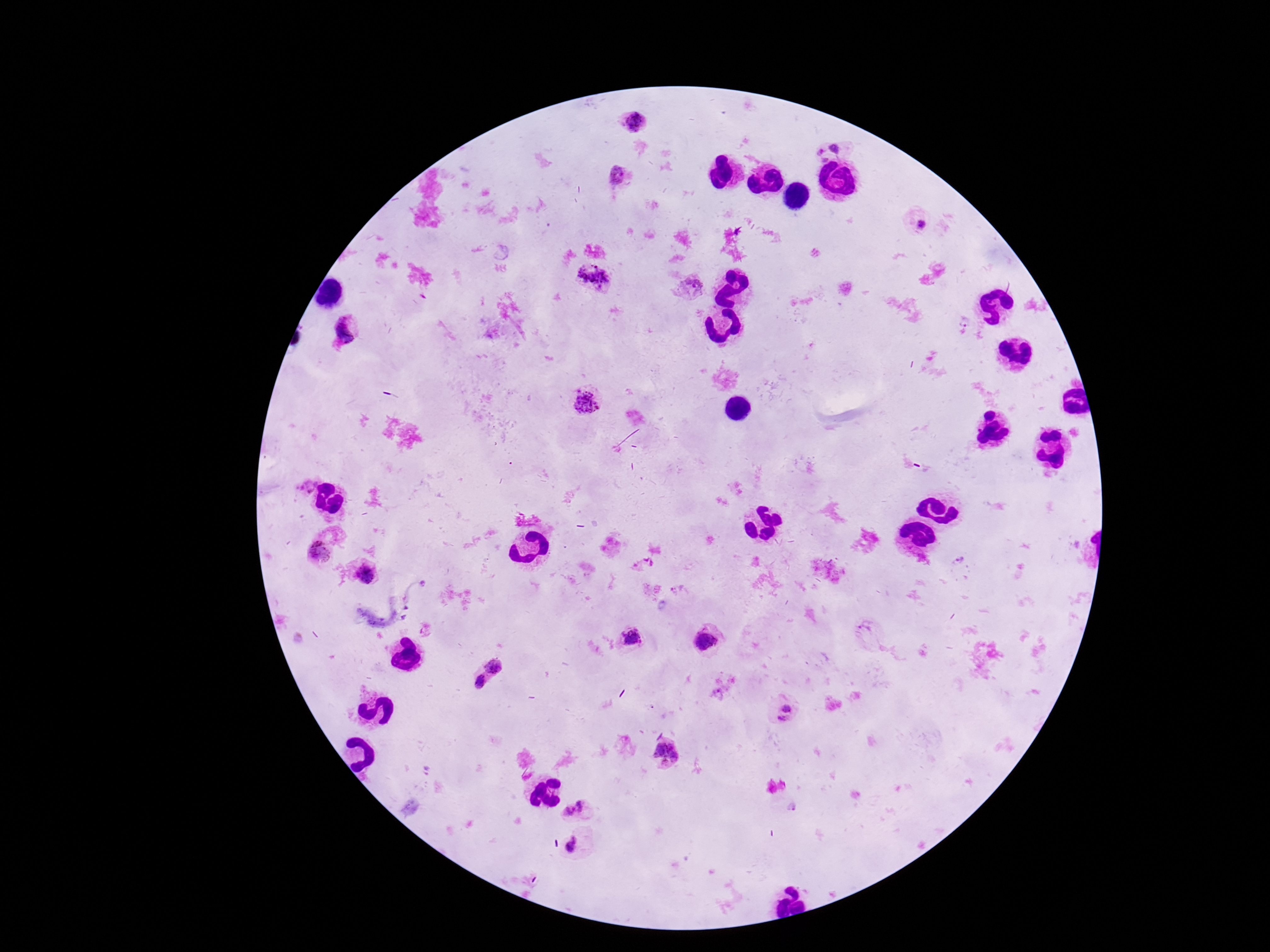

Approximate centers as (x, y) in pixels.
Summary:
  - Plasmodium parasite locations: (638, 125), (835, 148), (822, 156), (619, 178), (922, 224), (599, 279), (689, 290), (966, 320), (347, 330), (583, 403), (305, 484), (319, 553), (958, 562), (366, 574), (632, 638), (706, 641), (496, 660), (480, 684), (786, 711), (665, 752), (578, 809), (571, 846)
  - Preparation: thick blood smear
  - Patient malaria status: infected
  - Field of view: single
  - Capture: smartphone camera through the microscope eyepiece
  - Stain: Giemsa
  - Image size: 1270×952 pixels
  - Magnification: 100x